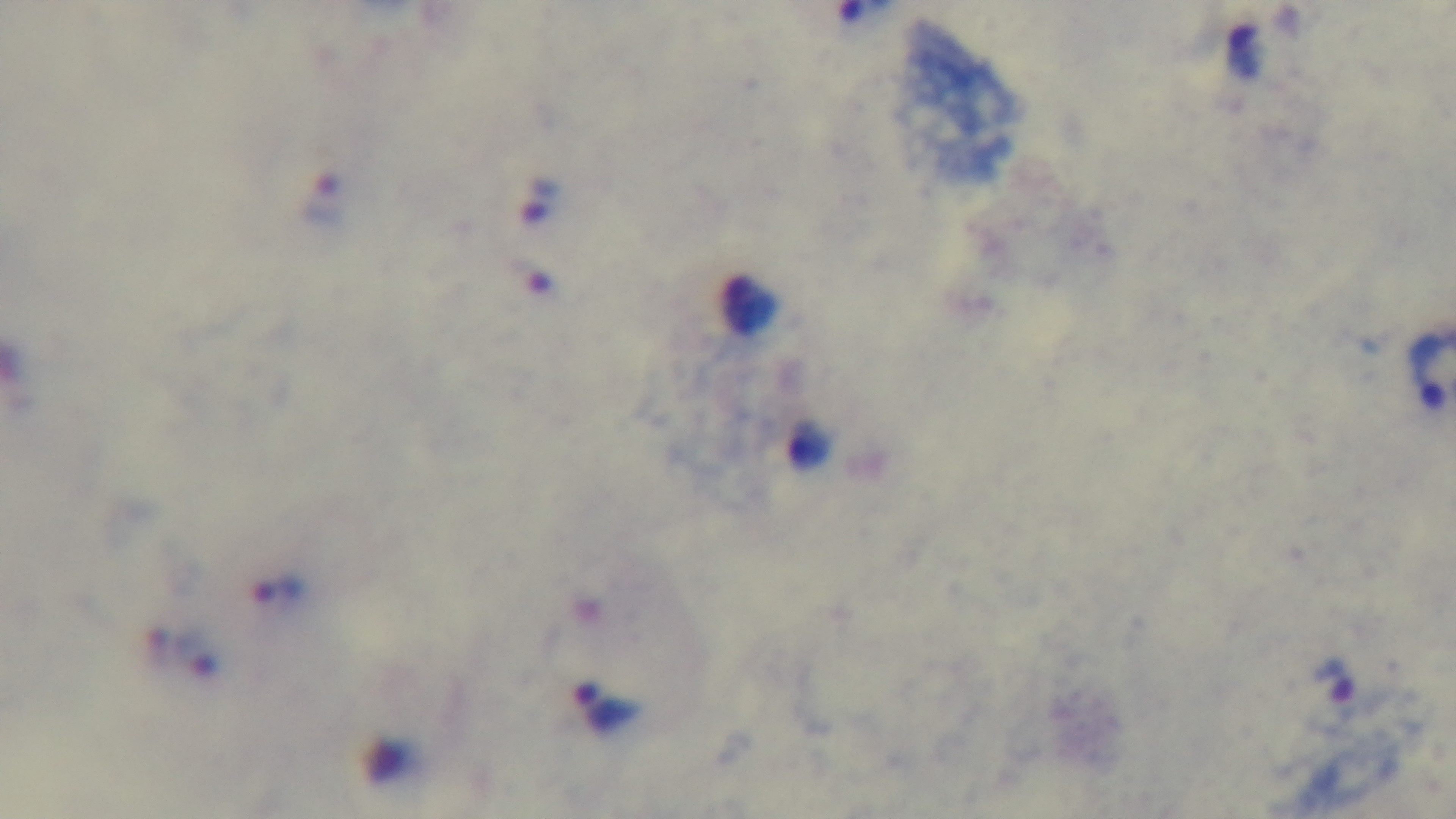
{
  "stain": "Giemsa",
  "modality": "light microscopy",
  "malaria_status": "positive",
  "objective": "100x oil immersion",
  "capture": "mounted 4K digital camera",
  "field_of_view": "one from the slide",
  "preparation": "thick smear"
}